Outline each blood parasite and name the species.
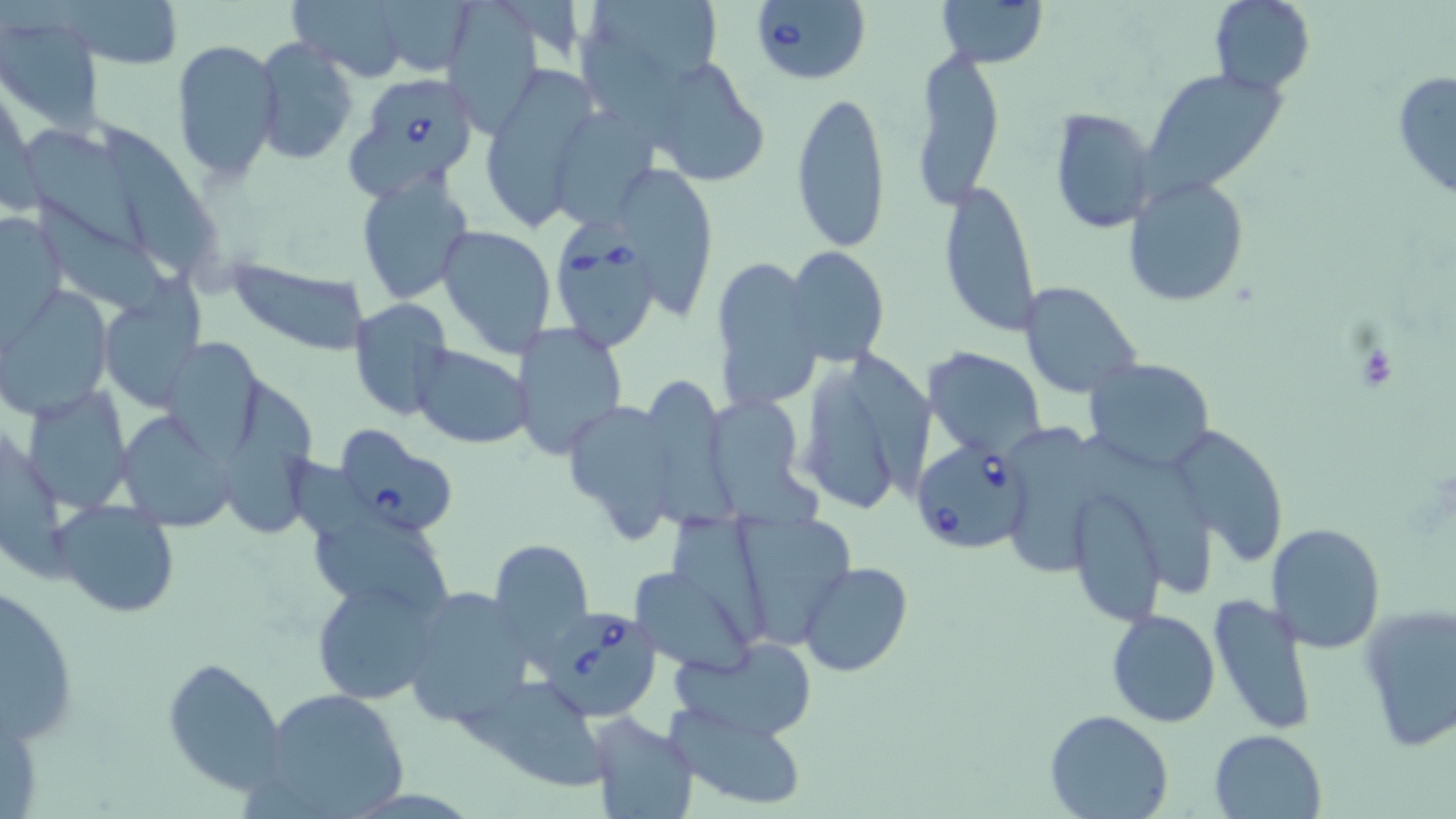

Approximate bounding boxes as named x1/y1/x2/y2 corners in pixels.
Babesia divergens-infected red blood cells: (x1=747, y1=0, x2=873, y2=86), (x1=346, y1=73, x2=482, y2=198), (x1=551, y1=233, x2=662, y2=352), (x1=334, y1=424, x2=459, y2=536), (x1=906, y1=433, x2=1033, y2=550), (x1=540, y1=598, x2=663, y2=720).
No Plasmodium falciparum, Plasmodium ovale, Plasmodium malariae, Plasmodium vivax, or Trypanosoma brucei observed.

Summary:
  - Uninfected red blood cell locations: (x1=60, y1=0, x2=184, y2=69), (x1=286, y1=0, x2=413, y2=82), (x1=447, y1=0, x2=544, y2=138), (x1=578, y1=0, x2=727, y2=103), (x1=937, y1=0, x2=1049, y2=69), (x1=1208, y1=0, x2=1315, y2=95), (x1=373, y1=1, x2=477, y2=73), (x1=0, y1=17, x2=103, y2=132), (x1=171, y1=38, x2=282, y2=184), (x1=253, y1=38, x2=358, y2=165), (x1=911, y1=48, x2=1005, y2=209), (x1=641, y1=56, x2=772, y2=187), (x1=1141, y1=66, x2=1288, y2=199), (x1=1393, y1=68, x2=1456, y2=198), (x1=476, y1=70, x2=598, y2=229), (x1=791, y1=86, x2=892, y2=255), (x1=547, y1=105, x2=659, y2=231), (x1=1048, y1=107, x2=1157, y2=231), (x1=103, y1=123, x2=217, y2=278), (x1=26, y1=128, x2=146, y2=253), (x1=627, y1=165, x2=715, y2=318), (x1=356, y1=173, x2=475, y2=306), (x1=1123, y1=175, x2=1250, y2=307), (x1=939, y1=177, x2=1042, y2=339), (x1=41, y1=201, x2=172, y2=319), (x1=0, y1=213, x2=65, y2=334), (x1=437, y1=225, x2=556, y2=358), (x1=786, y1=246, x2=889, y2=367), (x1=710, y1=256, x2=821, y2=414), (x1=225, y1=257, x2=370, y2=358), (x1=1019, y1=281, x2=1142, y2=397), (x1=4, y1=284, x2=113, y2=418), (x1=100, y1=287, x2=204, y2=412), (x1=349, y1=298, x2=455, y2=421), (x1=511, y1=323, x2=627, y2=459), (x1=160, y1=337, x2=266, y2=457), (x1=412, y1=344, x2=531, y2=448), (x1=925, y1=347, x2=1046, y2=459), (x1=794, y1=348, x2=933, y2=520), (x1=1083, y1=357, x2=1216, y2=473), (x1=651, y1=377, x2=747, y2=533), (x1=228, y1=381, x2=323, y2=534), (x1=23, y1=387, x2=132, y2=513), (x1=712, y1=401, x2=830, y2=529), (x1=563, y1=402, x2=678, y2=541), (x1=115, y1=412, x2=237, y2=531), (x1=1171, y1=421, x2=1292, y2=564), (x1=1010, y1=422, x2=1114, y2=572), (x1=1082, y1=438, x2=1211, y2=598), (x1=1063, y1=482, x2=1168, y2=626), (x1=50, y1=498, x2=182, y2=620), (x1=306, y1=509, x2=454, y2=617), (x1=727, y1=509, x2=859, y2=648), (x1=670, y1=514, x2=779, y2=647), (x1=1265, y1=522, x2=1387, y2=653), (x1=487, y1=540, x2=594, y2=654), (x1=799, y1=561, x2=915, y2=678), (x1=637, y1=565, x2=756, y2=678), (x1=310, y1=578, x2=439, y2=705), (x1=2, y1=583, x2=77, y2=745), (x1=400, y1=586, x2=533, y2=728), (x1=1208, y1=592, x2=1317, y2=735), (x1=1357, y1=603, x2=1455, y2=752), (x1=1105, y1=609, x2=1220, y2=728), (x1=676, y1=636, x2=817, y2=740), (x1=162, y1=653, x2=288, y2=796), (x1=469, y1=676, x2=609, y2=791), (x1=256, y1=684, x2=411, y2=818), (x1=667, y1=705, x2=811, y2=807), (x1=1046, y1=710, x2=1171, y2=819), (x1=584, y1=711, x2=698, y2=819), (x1=1209, y1=730, x2=1326, y2=819)
  - Slide-level diagnosis: Babesia divergens
  - Magnification: 1000x
  - Modality: optical microscopy
  - Image size: 1456×819 pixels
  - Preparation: thin blood smear
  - Stain: May-Grünwald-Giemsa
  - Field of view: one of a larger specimen